Assess this cell for malaria.
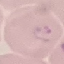
It is parasitized.

Giemsa-stained preparation. Automatically extracted cell patch, resized to 64 × 64 pixels. Acquired by smartphone through the microscope eyepiece. Thin blood smear.